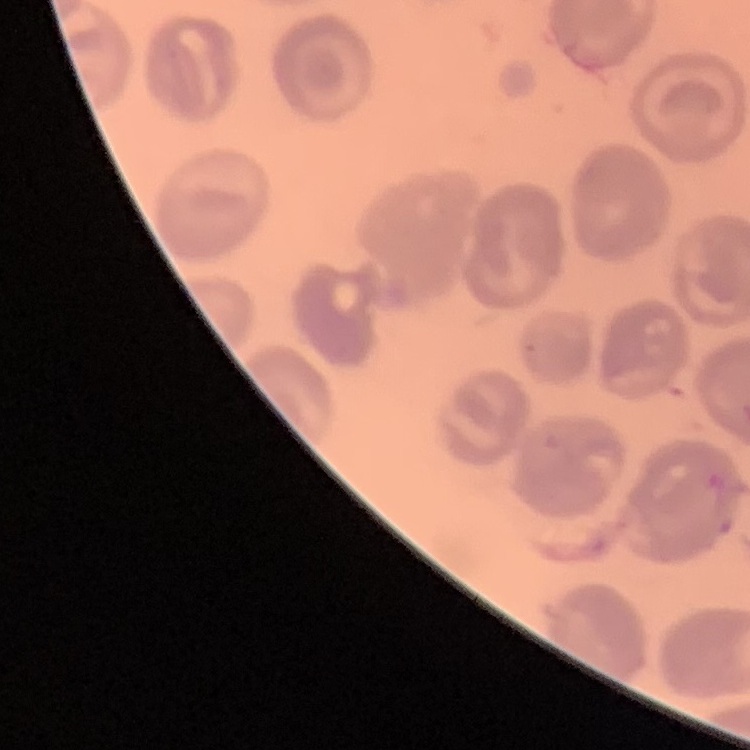
The erythrocytes exhibit no rouleaux formation. Square crop of a larger photomicrograph. Thin peripheral smear. Stained with either Field's or Giemsa.